Report the malaria status of this cell.
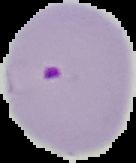

Parasitized.

preparation: thin blood smear
image_size: 136×163 pixels
image_type: cell region segmented out of the field of view; surrounding area masked to black